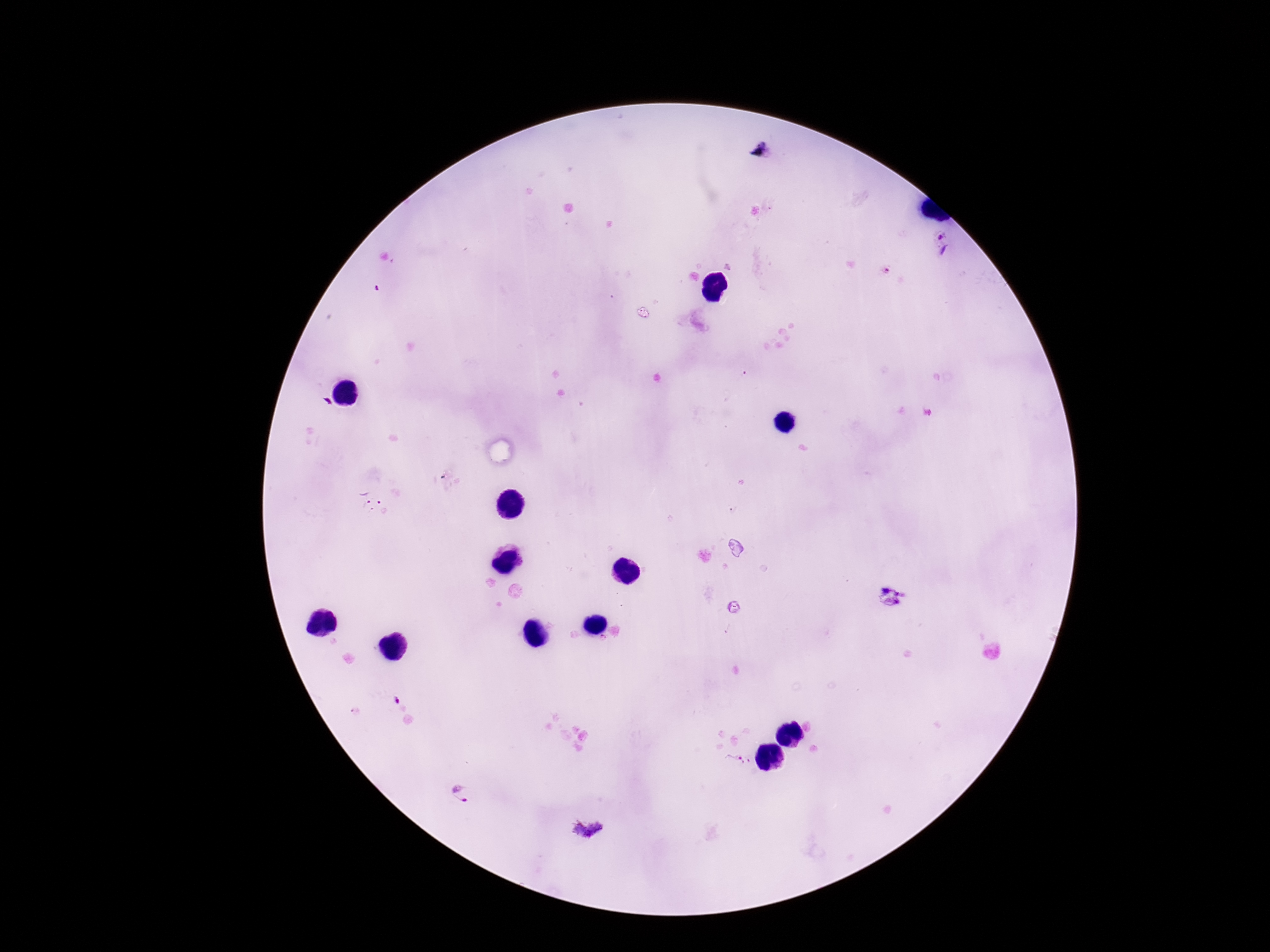 Approximate centers as [x, y] in pixels. Plasmodium parasite locations: [943, 241], [885, 271], [371, 500], [392, 700], [738, 762], [460, 795], [588, 830]. 100x magnification. Image is 1270×952 pixels. Single field of view. Patient malaria status: positive. Thick blood film. Giemsa stain. Photographed through the microscope eyepiece with a smartphone camera.